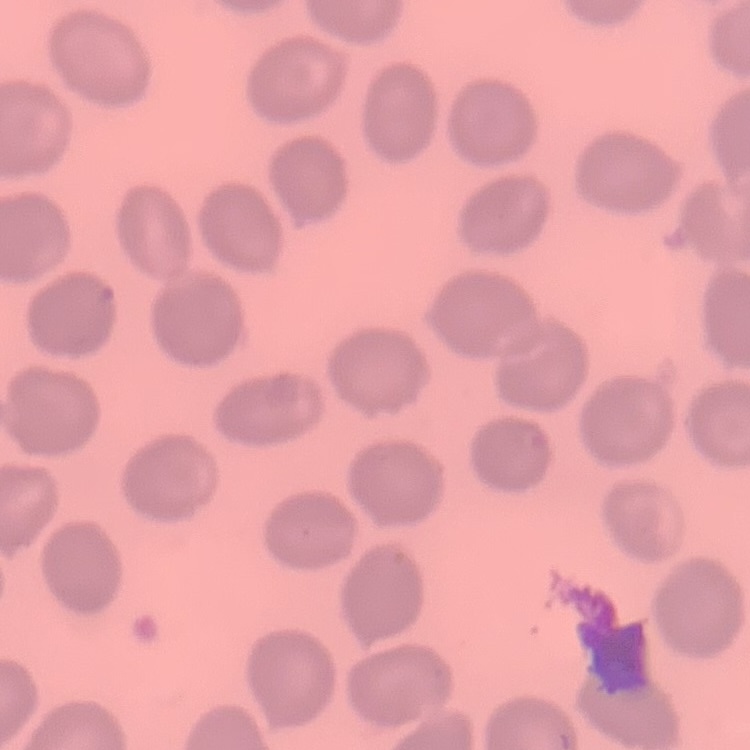 The red blood cells show no rouleaux formation. Square crop of a larger photomicrograph. Thin blood film. Field's or Giemsa stain.